Locate every uninfected red blood cell.
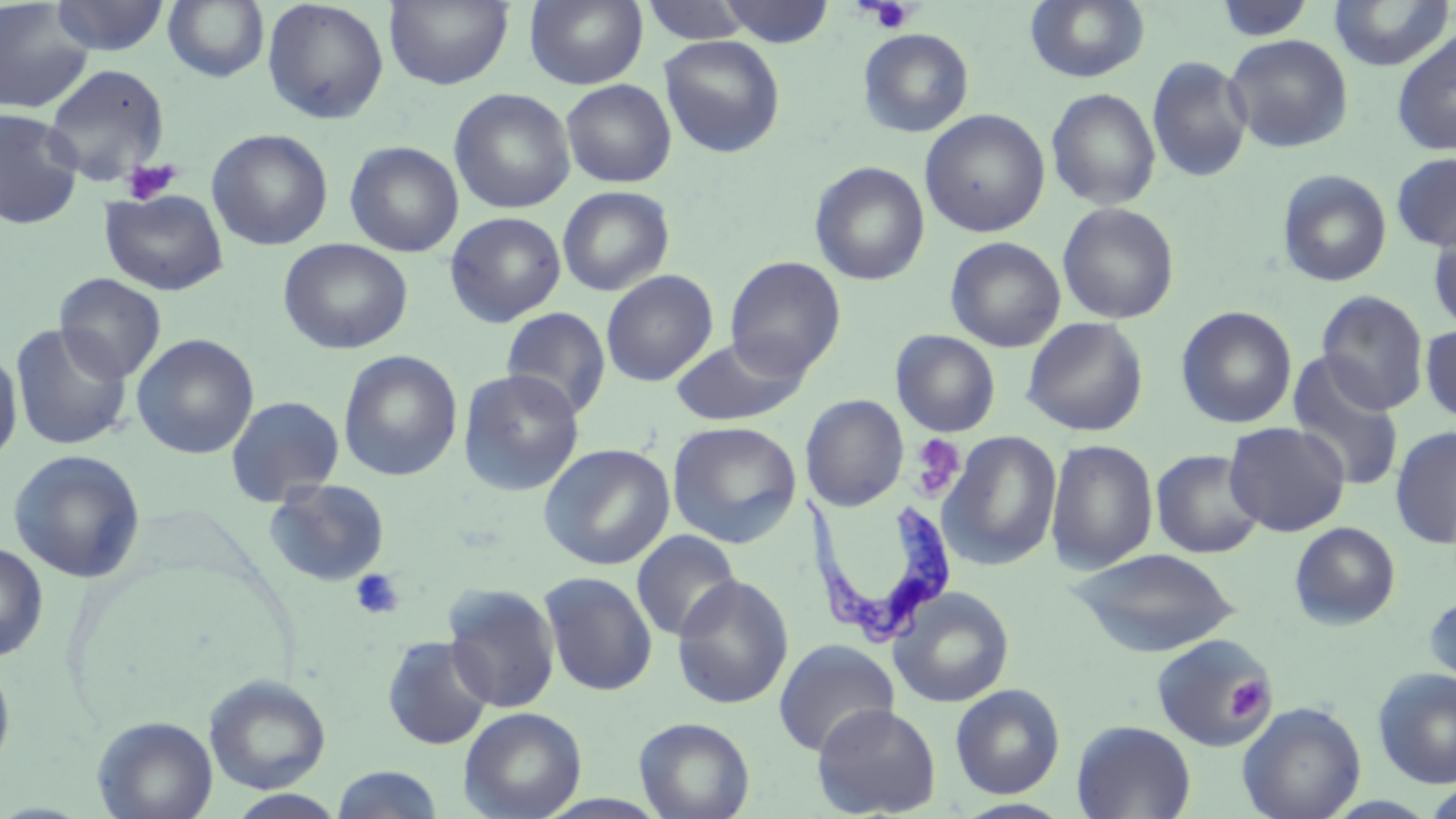
Approximate bounding boxes as named x1/y1/x2/y2 corners in pixels.
Uninfected red blood cells: (x1=0, y1=0, x2=95, y2=114), (x1=50, y1=0, x2=170, y2=56), (x1=163, y1=0, x2=270, y2=83), (x1=384, y1=0, x2=513, y2=90), (x1=525, y1=0, x2=648, y2=89), (x1=1025, y1=0, x2=1150, y2=83), (x1=1327, y1=0, x2=1455, y2=71), (x1=262, y1=1, x2=389, y2=124), (x1=639, y1=1, x2=755, y2=45), (x1=716, y1=1, x2=836, y2=47), (x1=1213, y1=1, x2=1318, y2=43), (x1=858, y1=28, x2=974, y2=137), (x1=1392, y1=29, x2=1456, y2=157), (x1=1224, y1=34, x2=1354, y2=153), (x1=658, y1=35, x2=785, y2=158), (x1=1147, y1=56, x2=1252, y2=183), (x1=41, y1=62, x2=171, y2=185), (x1=560, y1=78, x2=677, y2=188), (x1=448, y1=88, x2=576, y2=214), (x1=1046, y1=88, x2=1161, y2=210), (x1=0, y1=108, x2=83, y2=230), (x1=919, y1=109, x2=1050, y2=237), (x1=207, y1=129, x2=333, y2=250), (x1=345, y1=141, x2=464, y2=257), (x1=1391, y1=152, x2=1456, y2=252), (x1=809, y1=161, x2=930, y2=285), (x1=1277, y1=169, x2=1392, y2=287), (x1=557, y1=186, x2=675, y2=296), (x1=99, y1=189, x2=229, y2=296), (x1=1058, y1=202, x2=1180, y2=324), (x1=445, y1=211, x2=566, y2=327), (x1=1427, y1=219, x2=1456, y2=334), (x1=945, y1=236, x2=1066, y2=352), (x1=278, y1=238, x2=413, y2=355), (x1=724, y1=256, x2=846, y2=379), (x1=601, y1=270, x2=718, y2=386), (x1=54, y1=273, x2=167, y2=384), (x1=1316, y1=290, x2=1429, y2=415), (x1=1176, y1=306, x2=1297, y2=428), (x1=501, y1=308, x2=611, y2=419), (x1=1022, y1=317, x2=1149, y2=436), (x1=10, y1=323, x2=132, y2=451), (x1=1420, y1=324, x2=1456, y2=424), (x1=890, y1=329, x2=1001, y2=437), (x1=132, y1=333, x2=259, y2=459), (x1=669, y1=335, x2=808, y2=427), (x1=0, y1=346, x2=23, y2=469), (x1=337, y1=350, x2=463, y2=482), (x1=1286, y1=353, x2=1405, y2=492), (x1=458, y1=368, x2=586, y2=496), (x1=225, y1=394, x2=346, y2=506), (x1=801, y1=394, x2=908, y2=511), (x1=667, y1=420, x2=803, y2=548), (x1=1223, y1=422, x2=1350, y2=536), (x1=1391, y1=426, x2=1456, y2=550), (x1=940, y1=431, x2=1062, y2=570), (x1=1045, y1=438, x2=1159, y2=575), (x1=538, y1=442, x2=675, y2=570), (x1=7, y1=448, x2=146, y2=583), (x1=1150, y1=449, x2=1265, y2=559), (x1=263, y1=477, x2=391, y2=587), (x1=1289, y1=522, x2=1401, y2=630), (x1=631, y1=529, x2=742, y2=642), (x1=0, y1=542, x2=49, y2=662), (x1=1070, y1=547, x2=1240, y2=657), (x1=539, y1=571, x2=657, y2=697), (x1=672, y1=574, x2=794, y2=710), (x1=442, y1=584, x2=560, y2=713), (x1=889, y1=586, x2=1015, y2=707), (x1=1423, y1=591, x2=1456, y2=693), (x1=1151, y1=634, x2=1276, y2=753), (x1=381, y1=635, x2=495, y2=750), (x1=773, y1=639, x2=899, y2=757), (x1=0, y1=656, x2=16, y2=779), (x1=1373, y1=668, x2=1456, y2=789), (x1=204, y1=675, x2=331, y2=794), (x1=950, y1=683, x2=1065, y2=799), (x1=1238, y1=701, x2=1366, y2=819), (x1=811, y1=702, x2=941, y2=818), (x1=460, y1=706, x2=587, y2=819), (x1=93, y1=715, x2=218, y2=819), (x1=634, y1=716, x2=756, y2=819), (x1=1071, y1=719, x2=1196, y2=819), (x1=331, y1=766, x2=445, y2=818), (x1=226, y1=790, x2=348, y2=818).

slide_level_diagnosis: Trypanosoma brucei
modality: light microscopy
stain: May-Grünwald-Giemsa
field_of_view: single
image_size: 1456×819 pixels
preparation: thin blood smear
platelet_locations: 'approximate bounding boxes as named x1/y1/x2/y2 corners in pixels: (x1=867, y1=1, x2=915, y2=33), (x1=120, y1=158, x2=183, y2=204), (x1=910, y1=434, x2=964, y2=499), (x1=350, y1=568, x2=404, y2=620), (x1=1226, y1=676, x2=1272, y2=720)'
magnification: 1000x
trypanosoma_brucei_locations: 'approximate bounding boxes as named x1/y1/x2/y2 corners in pixels: (x1=808, y1=489, x2=959, y2=647)'